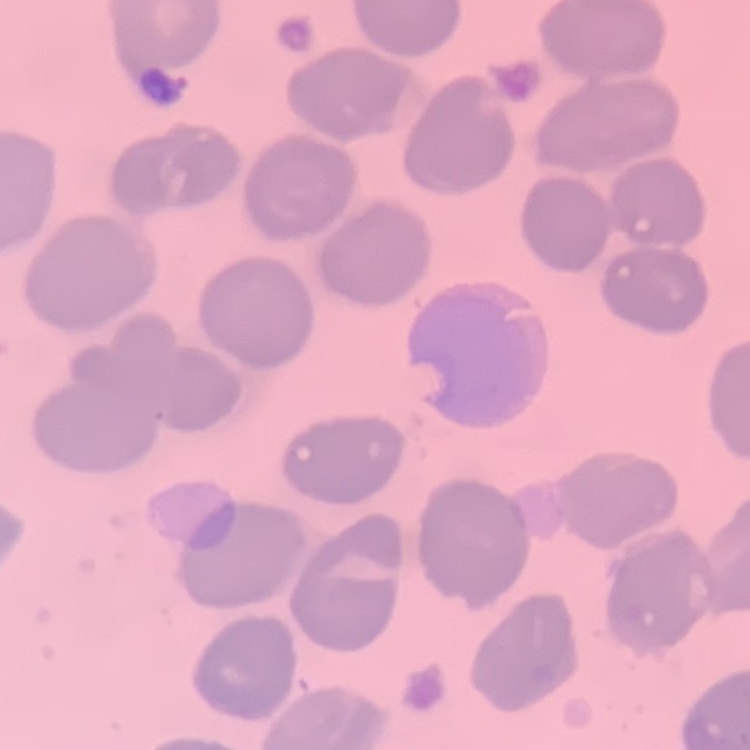

Summary:
  - Erythrocyte morphology: no rouleaux formation
  - Preparation: thin peripheral smear
  - Image type: one tile cut from a larger photomicrograph
  - Stain: Field's or Giemsa